Report the malaria status of this cell.
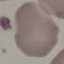
It is uninfected.

Giemsa-stained preparation. Thin blood smear. Acquired by smartphone through the microscope eyepiece. Automatically extracted cell patch, resized to 64 × 64 pixels.